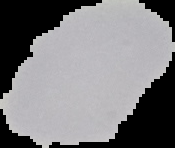

{
  "result": "no Plasmodium parasites detected",
  "preparation": "thin blood smear",
  "image_type": "segmented cell region on a black background",
  "image_size": "175×148 pixels"
}